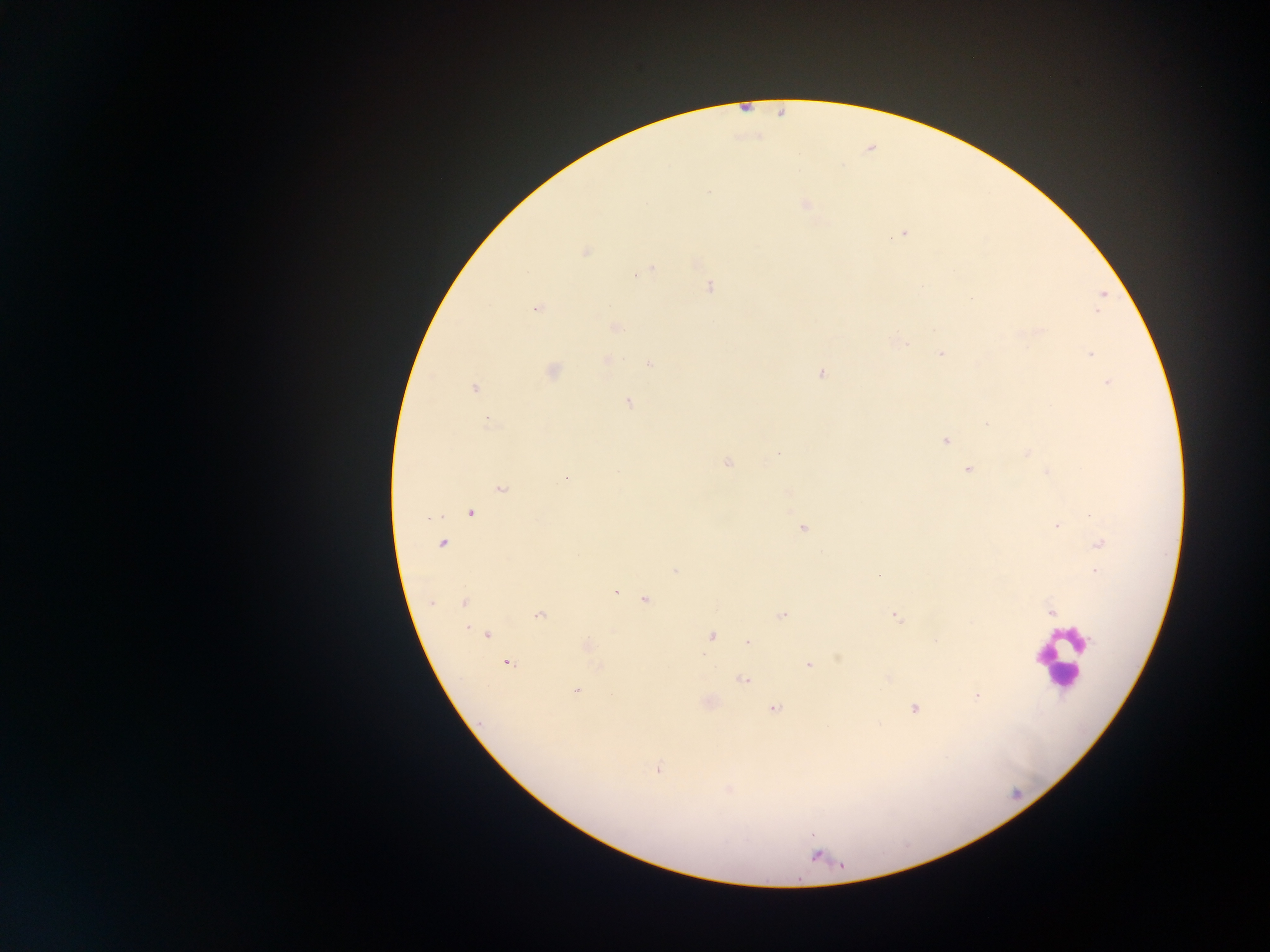
field of view = single
leukocyte locations = approximate centers as (x, y) in pixels: (1058, 658)
image size = 1270×952 pixels
preparation = thick blood film
capture = mobile-phone photograph through a microscope
malaria parasite locations = approximate centers as (x, y) in pixels: (708, 190), (805, 204), (903, 233), (585, 252), (652, 268), (643, 272), (636, 274), (710, 287), (1102, 295), (970, 299), (537, 308), (1098, 310), (616, 328), (941, 353), (1091, 354), (607, 360), (650, 364), (553, 371), (821, 373), (1107, 383), (474, 388), (628, 401), (488, 423), (987, 424), (945, 440), (778, 452), (1027, 452), (727, 463), (967, 470), (618, 471), (1047, 472), (565, 478), (501, 490), (471, 512), (428, 517), (1057, 526), (803, 528), (443, 543), (1100, 543), (675, 571), (1095, 572), (879, 577), (615, 592), (646, 599), (432, 603), (464, 603), (1051, 612), (539, 615), (782, 616), (896, 617), (468, 628), (488, 635), (712, 636), (747, 642), (587, 645), (508, 664), (808, 665), (600, 667), (742, 680), (576, 691), (976, 696), (775, 708), (914, 708), (658, 769), (814, 855)
country = Ghana